Name the blood parasite species.
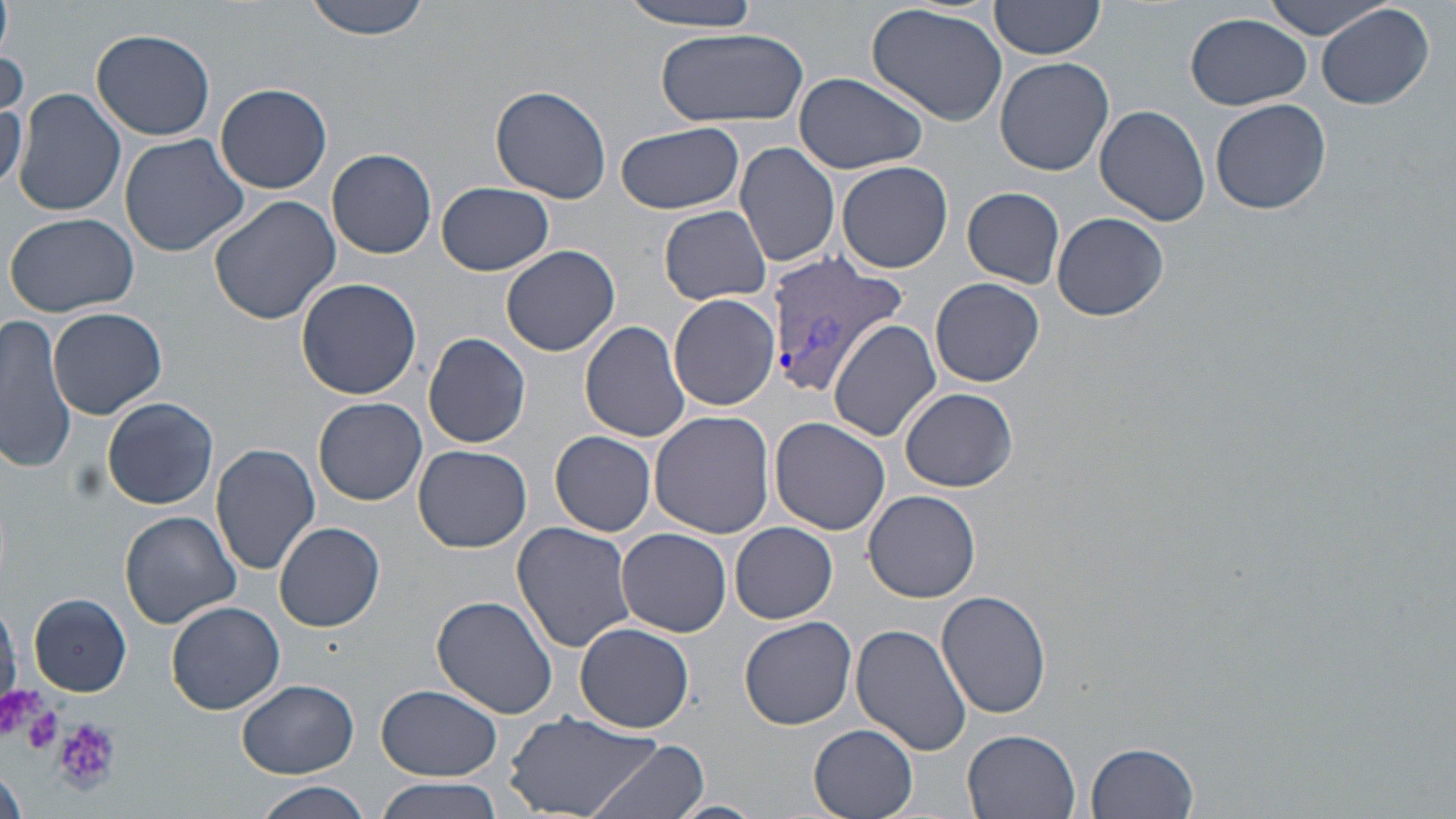
Plasmodium vivax.

Approximate bounding boxes as (x1, y1, x2, y2) in pixels. Uninfected red blood cell locations: (0, 0, 12, 57), (303, 0, 434, 41), (618, 0, 767, 29), (1264, 1, 1398, 40), (988, 2, 1107, 64), (1317, 3, 1435, 111), (866, 4, 1010, 129), (1185, 11, 1313, 110), (653, 26, 809, 127), (90, 28, 216, 141), (0, 38, 25, 121), (994, 57, 1113, 175), (793, 72, 928, 174), (216, 83, 332, 194), (490, 85, 613, 204), (14, 89, 126, 218), (1211, 97, 1332, 214), (0, 99, 27, 191), (1095, 104, 1210, 226), (616, 122, 746, 215), (117, 133, 250, 257), (734, 140, 841, 268), (326, 148, 438, 259), (837, 161, 954, 273), (437, 182, 555, 275), (963, 186, 1066, 288), (209, 194, 343, 324), (659, 206, 772, 305), (4, 211, 142, 315), (1053, 212, 1168, 321), (502, 246, 621, 356), (296, 276, 422, 400), (930, 278, 1044, 387), (668, 294, 779, 410), (47, 308, 166, 420), (0, 315, 76, 473), (580, 320, 694, 442), (830, 320, 942, 442), (423, 332, 532, 449), (899, 387, 1018, 492), (100, 396, 218, 510), (314, 398, 428, 505), (650, 411, 776, 540), (769, 416, 890, 534), (550, 431, 657, 535), (211, 442, 321, 575), (413, 444, 532, 553), (864, 489, 981, 602), (120, 511, 242, 628), (274, 522, 385, 632), (511, 522, 635, 653), (731, 523, 837, 623), (618, 529, 732, 638), (937, 589, 1054, 718), (28, 593, 132, 697), (432, 595, 560, 718), (165, 600, 286, 714), (738, 615, 857, 730), (575, 622, 694, 732), (851, 624, 972, 757), (237, 679, 358, 777), (375, 684, 503, 782), (505, 709, 668, 819), (808, 722, 919, 819), (962, 730, 1082, 819), (590, 739, 712, 819), (1084, 741, 1200, 819), (1, 768, 26, 819), (374, 779, 508, 819), (249, 782, 377, 819), (666, 799, 768, 819). Plasmodium vivax-infected red blood cell locations: (762, 255, 911, 400). Platelet locations: (0, 682, 46, 738), (22, 706, 62, 754), (54, 716, 121, 791). Thin blood film. Light microscopy. May-Grünwald-Giemsa stain. Single field of view. 1000x magnification. Image is 1456×819 pixels.